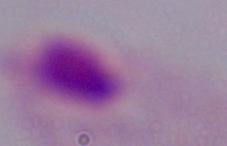

Summary:
  - Magnification: 1000x
  - Identification: trichomonad
  - Modality: micrograph